Name the parasite shown.
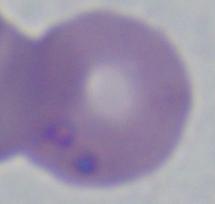
This is Babesia.

magnification = 1000x
modality = photomicrograph